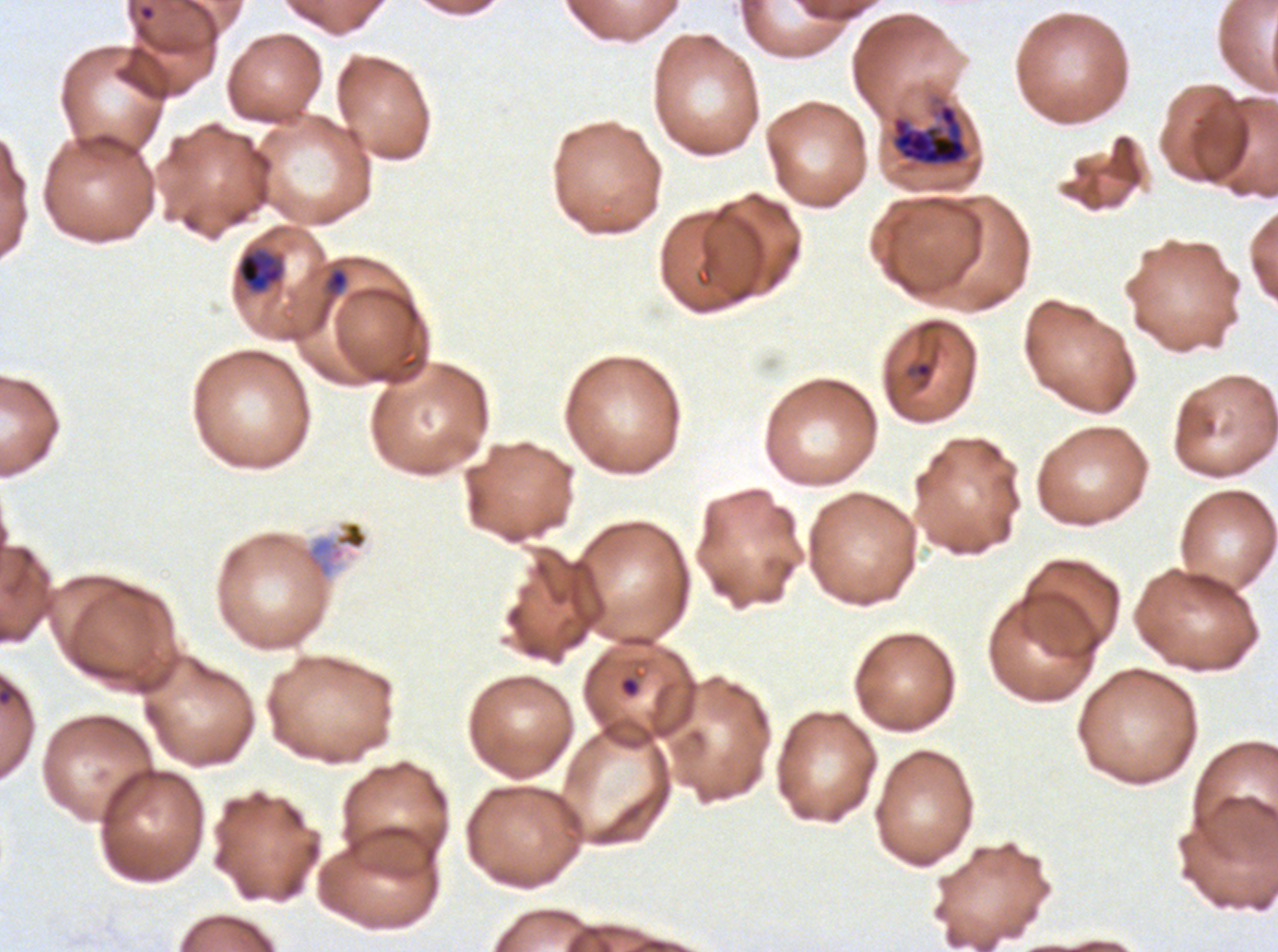

Approximate bounding boxes as [x1, y1, x2, y2] in pixels. Ring locations: [137, 3, 156, 22], [906, 360, 936, 390], [619, 676, 641, 698]. Early schizont locations: [891, 103, 969, 167]. Late-ring/early-trophozoite locations: [237, 251, 283, 292]. Debris locations: [303, 520, 368, 578]. Giemsa-stained preparation. One sub-image of a larger composite. P. falciparum from a patient in The Gambia, cultured ex vivo for 24 to 48 hours. Thin blood film. Image is 1278×952 pixels. Life-cycle stages observed: ring, late-ring/early-trophozoite, early schizont.